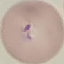
Malaria status: parasitized. Photographed with a smartphone camera at the microscope eyepiece. Thin blood film. Cell patch, automatically extracted from a larger field of view and resized to 64 × 64 pixels. Giemsa stain.